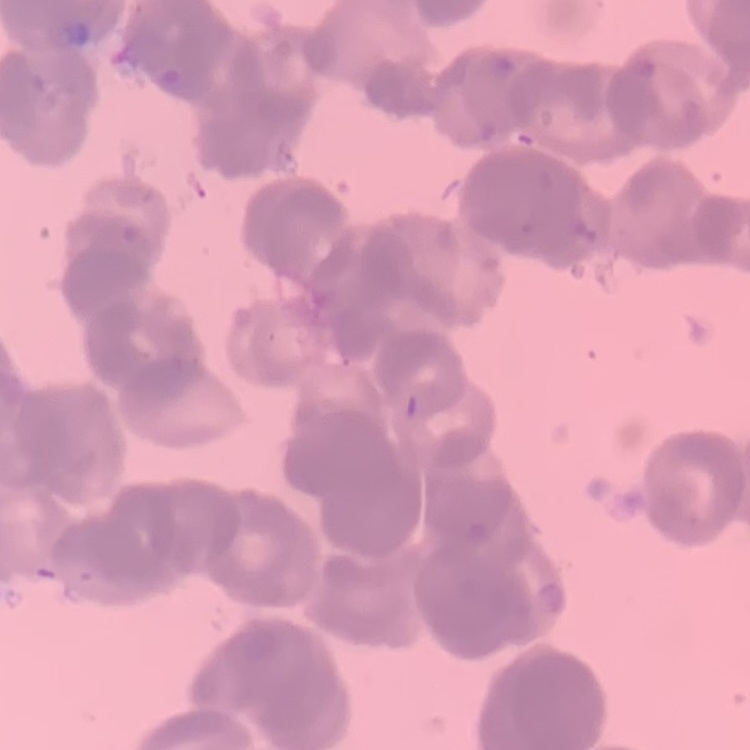

{
  "red_blood_cell_morphology": "rouleaux formation",
  "image_type": "one tile cut from a larger photomicrograph",
  "preparation": "thin blood smear",
  "stain": "Field's or Giemsa"
}